Classify this cell by malaria status.
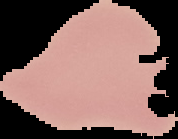
Uninfected.

Image is 178×139 pixels. Cell region segmented out of the field of view; the surrounding area is masked to black. From a thin blood smear.